Evaluate for Plasmodium parasites.
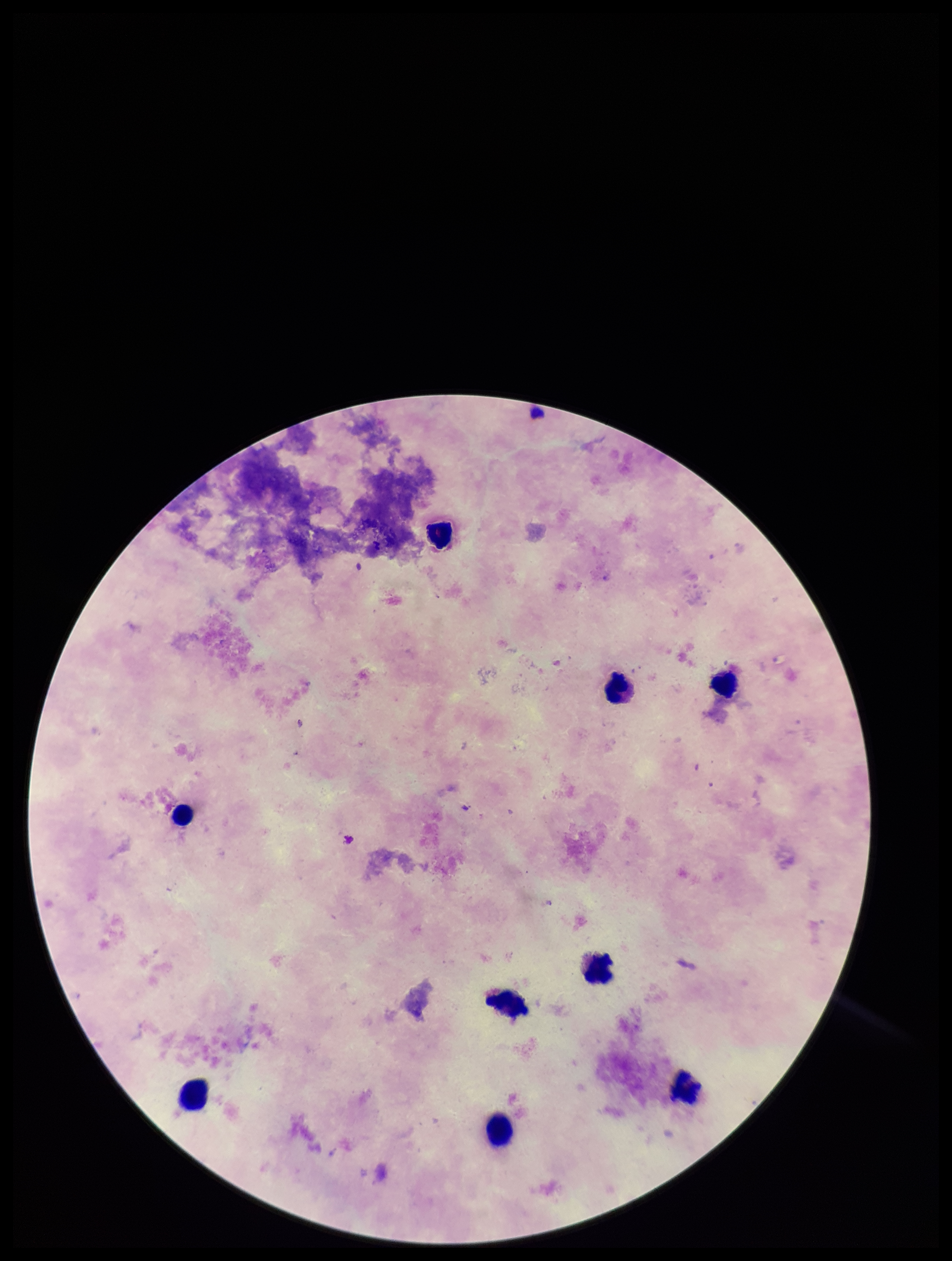

None detected.

Single field of view. Giemsa stain. Image is 952×1261 pixels. Patient malaria status: negative. Leukocyte count: 9. Preparation: thick smear. Parasite count: 0. Photographed through the microscope eyepiece with a smartphone camera.